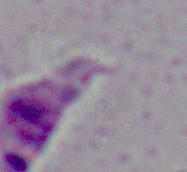
Summary:
  - Modality: photomicrograph
  - Identification: Leishmania
  - Magnification: 1000x